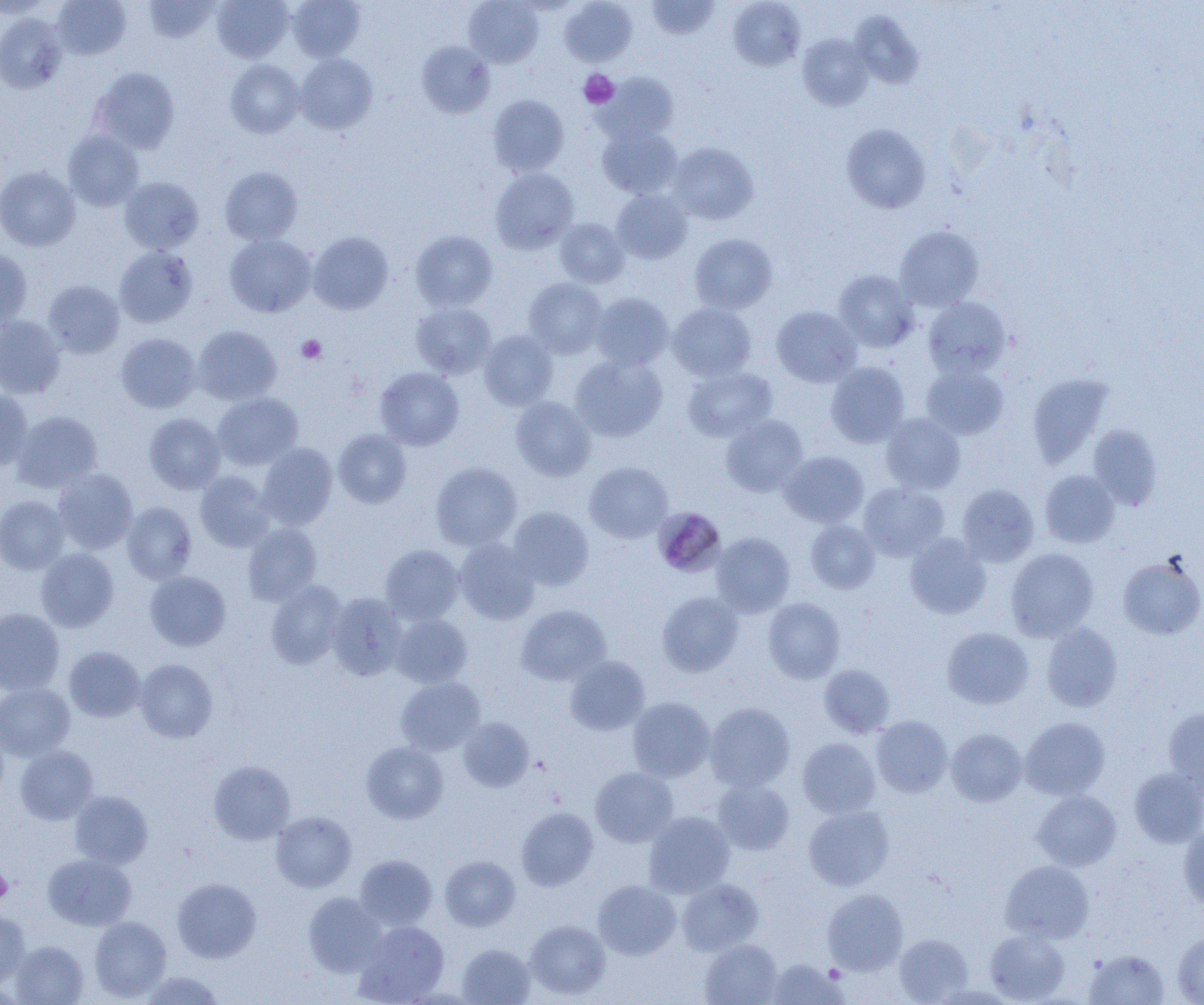

Summary:
  - Coordinate format: approximate bounding boxes as named x1/y1/x2/y2 corners in pixels
  - Plasmodium malariae-infected red blood cell locations: (x1=656, y1=509, x2=723, y2=575)
  - Platelet locations: (x1=579, y1=69, x2=619, y2=108), (x1=296, y1=335, x2=327, y2=363), (x1=0, y1=868, x2=13, y2=903)
  - Uninfected red blood cell locations: (x1=0, y1=0, x2=53, y2=19), (x1=52, y1=0, x2=131, y2=60), (x1=143, y1=0, x2=221, y2=43), (x1=212, y1=0, x2=294, y2=63), (x1=288, y1=0, x2=365, y2=61), (x1=463, y1=0, x2=543, y2=67), (x1=560, y1=0, x2=637, y2=66), (x1=646, y1=0, x2=719, y2=40), (x1=729, y1=1, x2=805, y2=71), (x1=849, y1=11, x2=923, y2=88), (x1=0, y1=13, x2=67, y2=93), (x1=798, y1=34, x2=873, y2=111), (x1=416, y1=41, x2=495, y2=118), (x1=295, y1=53, x2=377, y2=134), (x1=226, y1=59, x2=304, y2=138), (x1=91, y1=67, x2=180, y2=153), (x1=596, y1=73, x2=679, y2=145), (x1=488, y1=95, x2=569, y2=176), (x1=841, y1=123, x2=930, y2=214), (x1=597, y1=125, x2=682, y2=199), (x1=63, y1=130, x2=144, y2=211), (x1=668, y1=142, x2=758, y2=225), (x1=0, y1=166, x2=80, y2=251), (x1=220, y1=166, x2=303, y2=245), (x1=490, y1=168, x2=579, y2=253), (x1=119, y1=177, x2=204, y2=254), (x1=611, y1=189, x2=693, y2=264), (x1=555, y1=218, x2=629, y2=288), (x1=894, y1=225, x2=984, y2=311), (x1=411, y1=230, x2=497, y2=312), (x1=308, y1=231, x2=393, y2=315), (x1=689, y1=233, x2=778, y2=314), (x1=225, y1=234, x2=316, y2=317), (x1=113, y1=246, x2=197, y2=328), (x1=0, y1=249, x2=32, y2=330), (x1=834, y1=269, x2=919, y2=353), (x1=523, y1=277, x2=608, y2=359), (x1=43, y1=280, x2=124, y2=359), (x1=591, y1=292, x2=673, y2=370), (x1=923, y1=297, x2=1011, y2=378), (x1=411, y1=302, x2=496, y2=379), (x1=667, y1=302, x2=756, y2=383), (x1=772, y1=306, x2=861, y2=387), (x1=0, y1=315, x2=65, y2=399), (x1=193, y1=325, x2=281, y2=405), (x1=479, y1=329, x2=558, y2=411), (x1=116, y1=333, x2=201, y2=413), (x1=570, y1=354, x2=667, y2=442), (x1=826, y1=362, x2=910, y2=447), (x1=921, y1=364, x2=1009, y2=440), (x1=375, y1=367, x2=464, y2=451), (x1=682, y1=367, x2=777, y2=442), (x1=1027, y1=373, x2=1114, y2=468), (x1=0, y1=389, x2=33, y2=470), (x1=212, y1=392, x2=303, y2=470), (x1=510, y1=396, x2=596, y2=481), (x1=11, y1=411, x2=103, y2=494), (x1=144, y1=413, x2=226, y2=494), (x1=880, y1=413, x2=965, y2=494), (x1=721, y1=414, x2=808, y2=497), (x1=1088, y1=425, x2=1164, y2=510), (x1=333, y1=429, x2=411, y2=508), (x1=257, y1=443, x2=337, y2=529), (x1=780, y1=451, x2=869, y2=528), (x1=584, y1=461, x2=672, y2=543), (x1=431, y1=462, x2=521, y2=550), (x1=52, y1=468, x2=138, y2=555), (x1=1040, y1=470, x2=1120, y2=548), (x1=195, y1=471, x2=275, y2=551), (x1=858, y1=482, x2=950, y2=561), (x1=956, y1=484, x2=1039, y2=567), (x1=0, y1=495, x2=69, y2=574), (x1=122, y1=501, x2=197, y2=584), (x1=507, y1=506, x2=594, y2=591), (x1=806, y1=520, x2=880, y2=594), (x1=243, y1=523, x2=322, y2=605), (x1=711, y1=532, x2=795, y2=617), (x1=905, y1=534, x2=991, y2=619), (x1=454, y1=538, x2=540, y2=625), (x1=380, y1=544, x2=464, y2=624), (x1=36, y1=548, x2=119, y2=632), (x1=1005, y1=548, x2=1099, y2=642), (x1=1117, y1=555, x2=1204, y2=640), (x1=145, y1=571, x2=231, y2=651), (x1=266, y1=580, x2=348, y2=669), (x1=327, y1=592, x2=407, y2=680), (x1=657, y1=592, x2=744, y2=677), (x1=763, y1=597, x2=845, y2=683), (x1=516, y1=604, x2=611, y2=686), (x1=0, y1=608, x2=64, y2=694), (x1=391, y1=613, x2=472, y2=688), (x1=1041, y1=622, x2=1123, y2=712), (x1=941, y1=627, x2=1034, y2=709), (x1=64, y1=646, x2=146, y2=722), (x1=565, y1=655, x2=649, y2=736), (x1=134, y1=659, x2=217, y2=742), (x1=819, y1=664, x2=895, y2=738), (x1=396, y1=677, x2=485, y2=755), (x1=0, y1=683, x2=75, y2=761), (x1=627, y1=697, x2=715, y2=781), (x1=705, y1=702, x2=795, y2=791), (x1=1164, y1=707, x2=1204, y2=795), (x1=871, y1=715, x2=952, y2=797), (x1=1020, y1=716, x2=1110, y2=800), (x1=458, y1=717, x2=534, y2=792), (x1=0, y1=724, x2=9, y2=802), (x1=946, y1=728, x2=1027, y2=806), (x1=797, y1=737, x2=880, y2=818), (x1=361, y1=742, x2=448, y2=824), (x1=15, y1=745, x2=98, y2=824), (x1=209, y1=760, x2=295, y2=844), (x1=590, y1=767, x2=678, y2=847), (x1=1129, y1=768, x2=1204, y2=848), (x1=712, y1=778, x2=794, y2=855), (x1=70, y1=790, x2=153, y2=869), (x1=1032, y1=790, x2=1121, y2=871), (x1=803, y1=805, x2=894, y2=891), (x1=516, y1=808, x2=598, y2=891), (x1=271, y1=810, x2=356, y2=892), (x1=643, y1=811, x2=735, y2=898), (x1=1178, y1=822, x2=1204, y2=910), (x1=43, y1=853, x2=136, y2=930), (x1=354, y1=855, x2=437, y2=930), (x1=440, y1=856, x2=520, y2=931), (x1=1000, y1=860, x2=1094, y2=943), (x1=172, y1=878, x2=261, y2=963), (x1=677, y1=878, x2=763, y2=955), (x1=592, y1=880, x2=681, y2=959), (x1=822, y1=889, x2=908, y2=975), (x1=303, y1=892, x2=386, y2=977), (x1=0, y1=910, x2=31, y2=988), (x1=89, y1=916, x2=171, y2=1001), (x1=524, y1=919, x2=611, y2=1000), (x1=355, y1=920, x2=449, y2=1004), (x1=984, y1=928, x2=1069, y2=1004), (x1=1172, y1=931, x2=1204, y2=1004), (x1=894, y1=933, x2=973, y2=1003), (x1=700, y1=938, x2=783, y2=1005), (x1=9, y1=941, x2=88, y2=1005), (x1=457, y1=944, x2=536, y2=1005), (x1=1084, y1=949, x2=1169, y2=1005), (x1=766, y1=958, x2=847, y2=1004), (x1=142, y1=971, x2=223, y2=1005)
  - Slide-level diagnosis: Plasmodium malariae
  - Preparation: thin blood film
  - Magnification: 1000x
  - Field of view: single
  - Modality: optical microscopy
  - Image size: 1204×1005 pixels